Identify the parasite.
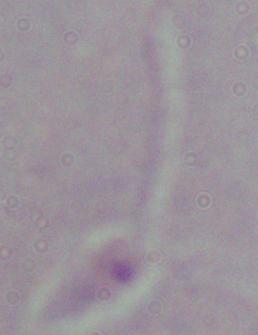
This is Leishmania.

Summary:
  - Magnification: 1000x
  - Modality: micrograph